Point out every malaria parasite.
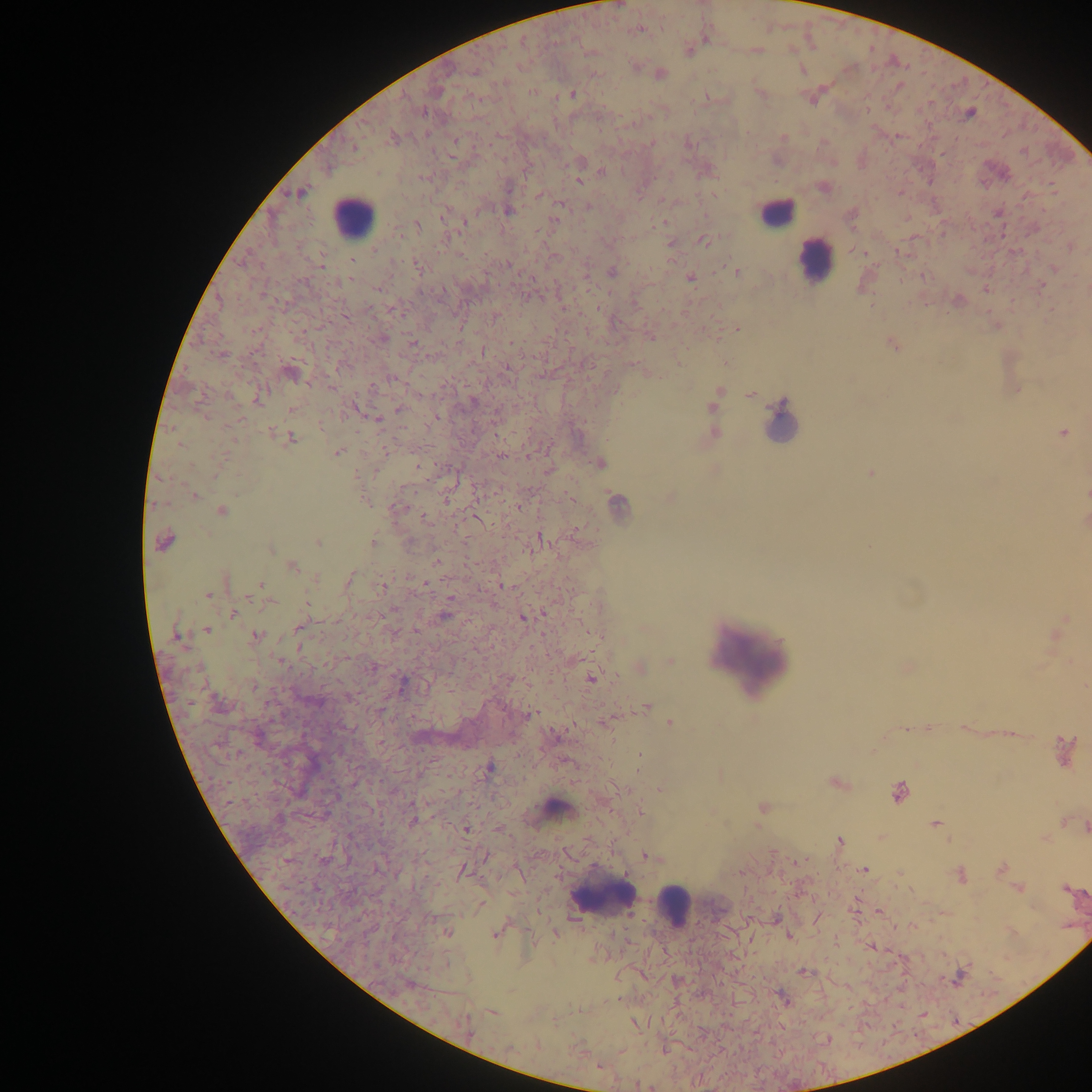
Approximate centers as [x, y] in pixels.
Malaria parasites: [641, 31], [758, 51], [803, 70], [899, 86], [533, 92], [760, 93], [573, 94], [705, 96], [812, 100], [932, 101], [867, 108], [424, 112], [918, 112], [969, 115], [747, 134], [897, 135], [782, 138], [454, 140], [651, 141], [602, 171], [419, 179], [578, 181], [539, 195], [898, 195], [661, 199], [561, 205], [587, 208], [508, 211], [665, 222], [465, 223], [418, 224], [398, 235], [444, 239], [703, 240], [896, 251], [323, 252], [350, 262], [508, 265], [874, 265], [323, 266], [417, 268], [1053, 270], [611, 272], [738, 273], [690, 277], [351, 278], [1041, 285], [376, 289], [443, 290], [563, 307], [597, 308], [393, 310], [497, 317], [737, 330], [510, 343], [508, 368], [392, 380], [310, 383], [370, 387], [331, 388], [257, 400], [472, 401], [712, 406], [290, 409], [399, 409], [436, 416], [493, 416], [206, 417], [241, 420], [379, 421], [320, 426], [401, 429], [271, 432], [1061, 433], [290, 437], [235, 441], [179, 445], [386, 451], [337, 453], [529, 455], [500, 456], [225, 458], [417, 465], [357, 473], [497, 492], [195, 495], [569, 497], [363, 500], [445, 501], [155, 503], [518, 507], [399, 508], [222, 510], [424, 518], [578, 528], [538, 535], [166, 541], [372, 542], [318, 543], [271, 550], [436, 561], [292, 567], [405, 575], [348, 579], [261, 584], [425, 584], [501, 584], [384, 585], [411, 593], [209, 596], [450, 598], [248, 599], [268, 603], [306, 603], [233, 613], [523, 619], [297, 629], [416, 630], [208, 631], [256, 634], [300, 647], [281, 660], [590, 678], [348, 697], [647, 706], [531, 714], [671, 723], [961, 727], [927, 728], [906, 729], [1012, 734], [1064, 751], [239, 753], [638, 755], [488, 767], [638, 769], [896, 791], [228, 802], [412, 821], [933, 823], [1084, 825], [466, 830], [839, 841], [645, 855], [1001, 868], [463, 869], [863, 869], [1018, 888], [1063, 888], [878, 912], [817, 919], [913, 926], [447, 933], [495, 935], [788, 936], [871, 948], [800, 971], [618, 999], [597, 1067].

Leukocyte locations: [782, 207], [348, 212], [821, 263], [749, 663], [557, 805], [601, 903], [679, 913]. Sample from Ghana. Image is 1092×1092 pixels. Single field of view. Thick blood film. Mobile-phone photograph taken through the microscope.